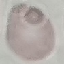

Malaria status: uninfected. Cell patch, automatically extracted from a larger field of view and resized to 64 × 64 pixels. Acquired by smartphone through the microscope eyepiece. Thin smear of blood. Giemsa-stained preparation.